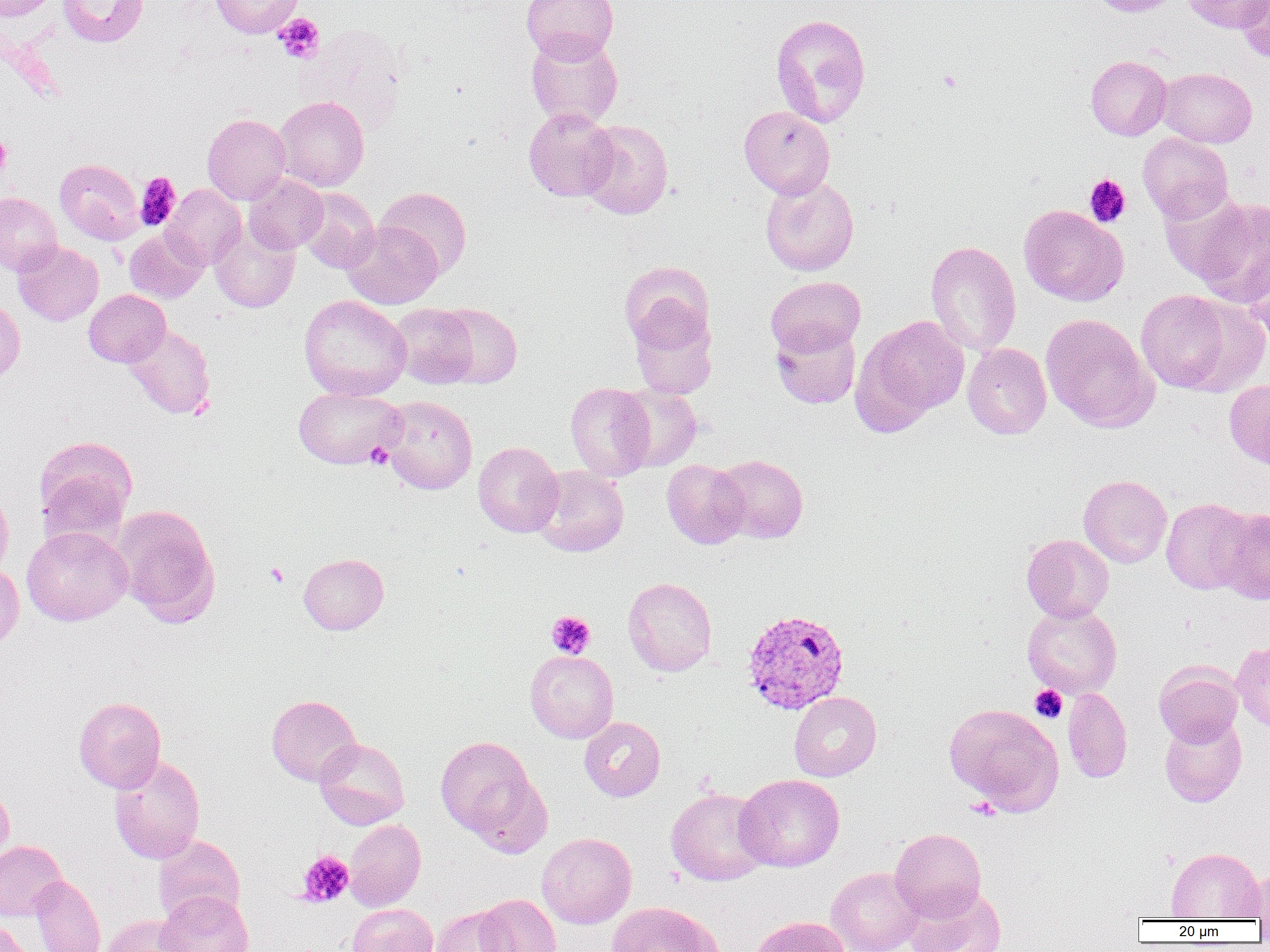
Summary:
  - Coordinate format: approximate bounding boxes as (x1, y1, x2, y2) in pixels
  - Uninfected red blood cell locations: (0, 0, 59, 22), (57, 0, 149, 47), (210, 0, 303, 38), (521, 0, 619, 63), (1088, 0, 1181, 16), (1181, 0, 1267, 33), (1236, 0, 1270, 62), (770, 13, 871, 127), (526, 31, 623, 129), (1085, 56, 1171, 140), (1157, 67, 1257, 148), (274, 95, 369, 191), (739, 106, 835, 199), (524, 108, 618, 201), (202, 113, 291, 205), (579, 119, 674, 219), (1138, 132, 1234, 223), (55, 158, 144, 244), (243, 173, 328, 254), (760, 175, 859, 276), (162, 184, 246, 270), (376, 186, 472, 278), (296, 188, 380, 273), (1159, 188, 1253, 285), (0, 192, 62, 276), (1191, 197, 1270, 306), (1019, 205, 1128, 306), (342, 221, 442, 309), (210, 224, 299, 313), (124, 229, 207, 303), (926, 240, 1021, 357), (13, 241, 104, 326), (1244, 246, 1270, 348), (619, 261, 714, 352), (766, 276, 865, 357), (84, 289, 171, 367), (1135, 290, 1240, 393), (299, 295, 411, 401), (0, 297, 25, 383), (389, 303, 480, 389), (434, 304, 522, 389), (629, 304, 718, 399), (1040, 313, 1158, 433), (857, 315, 970, 424), (771, 323, 861, 408), (122, 324, 216, 419), (963, 343, 1051, 439), (1224, 379, 1270, 470), (566, 382, 655, 481), (616, 385, 702, 472), (293, 386, 407, 469), (381, 395, 477, 494), (34, 435, 137, 539), (473, 441, 564, 537), (713, 454, 809, 544), (662, 459, 750, 549), (532, 465, 629, 557), (1079, 475, 1171, 568), (0, 486, 14, 579), (1160, 498, 1254, 594), (110, 504, 220, 626), (1214, 507, 1270, 604), (22, 526, 132, 626), (1021, 534, 1114, 622), (298, 553, 388, 635), (0, 563, 24, 656), (623, 576, 717, 677), (1022, 603, 1122, 699), (1232, 641, 1270, 732), (525, 650, 618, 743), (1154, 662, 1243, 746), (1063, 688, 1132, 783), (789, 692, 882, 781), (266, 694, 362, 786), (73, 696, 166, 792), (943, 703, 1063, 814), (1160, 715, 1247, 807), (579, 717, 665, 802), (436, 735, 542, 843), (314, 738, 410, 829), (109, 754, 206, 864), (735, 774, 844, 872), (0, 781, 14, 865), (666, 787, 772, 886), (344, 818, 426, 911), (890, 828, 986, 920), (537, 832, 637, 928), (153, 835, 245, 925), (0, 840, 68, 921), (1166, 847, 1264, 920), (826, 866, 923, 952), (1239, 867, 1270, 919), (30, 875, 105, 952), (903, 885, 1006, 952), (156, 890, 253, 952), (474, 894, 562, 952), (607, 901, 723, 952), (346, 903, 438, 952), (430, 906, 515, 952), (102, 915, 193, 952), (748, 916, 849, 952), (0, 917, 31, 952)
  - Platelet locations: (274, 13, 325, 63), (937, 70, 961, 92), (0, 135, 11, 177), (135, 173, 181, 231), (1084, 174, 1131, 227), (365, 443, 394, 469), (265, 562, 289, 587), (546, 611, 595, 658), (1030, 685, 1067, 723), (297, 850, 354, 907)
  - Plasmodium vivax-infected red blood cell locations: (741, 608, 850, 714)
  - Slide-level diagnosis: Plasmodium vivax
  - Modality: light microscopy
  - Preparation: thin blood smear
  - Magnification: 1000x
  - Field of view: one of a larger specimen
  - Image size: 1270×952 pixels